Assess the morphology of the erythrocytes.
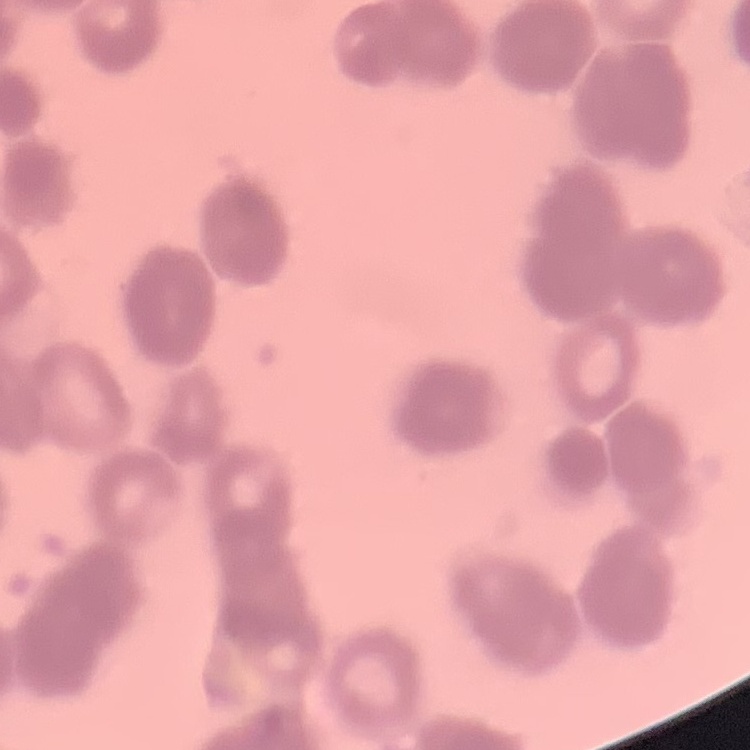
Rouleaux formation.

Summary:
  - Preparation: thin peripheral smear
  - Stain: Field's or Giemsa
  - Image type: one tile cut from a larger photomicrograph